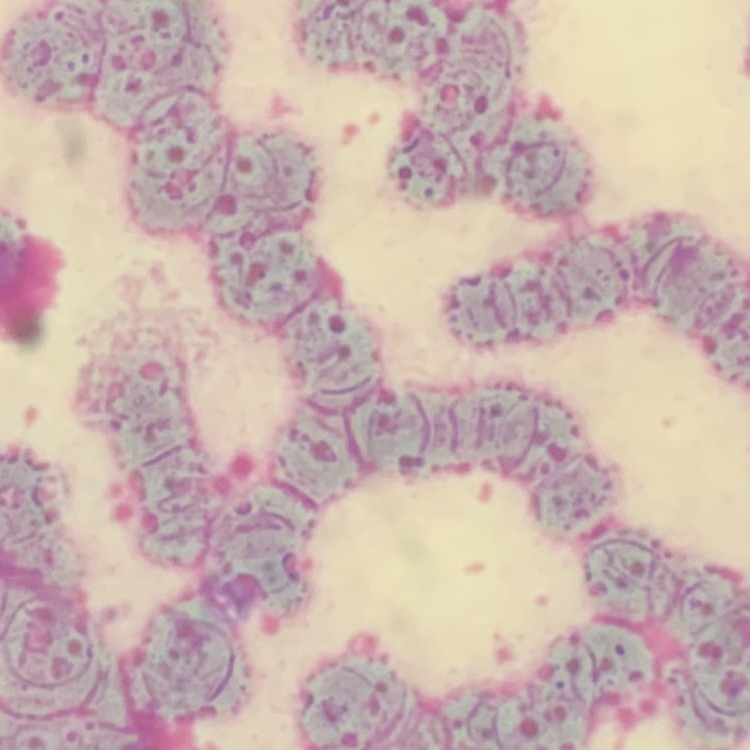

Summary:
  - Red blood cell morphology: rouleaux formation
  - Stain: Field's or Giemsa
  - Preparation: thin blood film
  - Image type: square crop of a larger photomicrograph